Assess this cell for malaria.
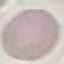

Uninfected.

capture = smartphone through the microscope eyepiece
image type = automatically extracted cell patch, resized to 64 × 64 pixels
preparation = thin smear
stain = Giemsa